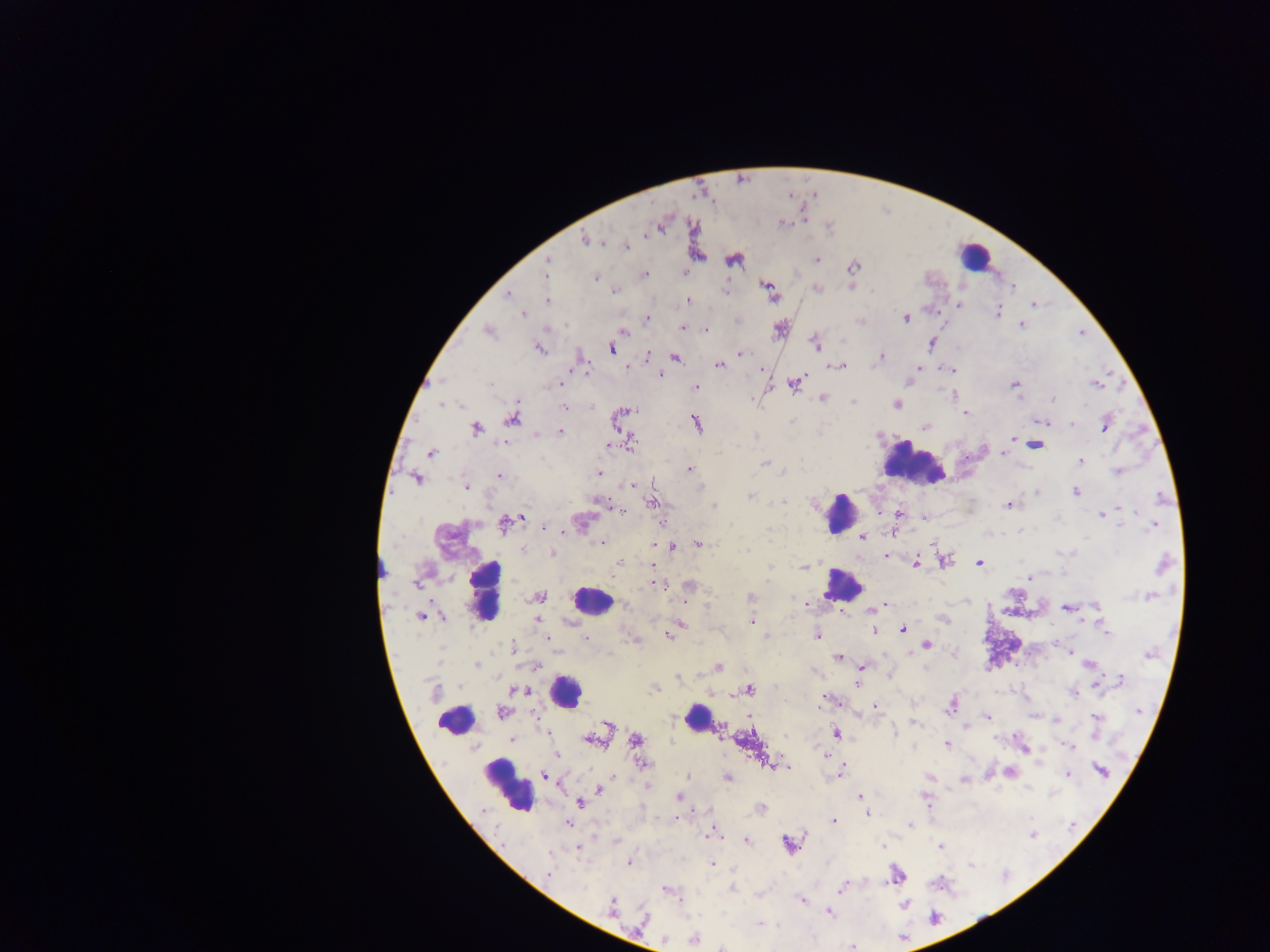

Approximate centers as {x, y} in pixels.
Summary:
  - Malaria parasite locations: {782, 223}, {585, 239}, {626, 246}, {733, 260}, {816, 260}, {547, 265}, {852, 267}, {685, 272}, {545, 274}, {644, 275}, {596, 278}, {852, 287}, {768, 288}, {817, 288}, {726, 290}, {615, 291}, {507, 294}, {772, 294}, {547, 301}, {688, 301}, {959, 304}, {1034, 305}, {998, 312}, {523, 314}, {906, 318}, {647, 319}, {860, 321}, {1022, 324}, {683, 328}, {780, 328}, {705, 329}, {489, 332}, {623, 332}, {816, 343}, {931, 343}, {539, 349}, {612, 349}, {742, 354}, {646, 357}, {675, 357}, {881, 357}, {719, 365}, {840, 366}, {628, 367}, {917, 367}, {473, 369}, {951, 370}, {660, 375}, {562, 380}, {441, 381}, {559, 384}, {795, 384}, {1096, 384}, {1014, 385}, {696, 387}, {823, 397}, {1053, 398}, {853, 402}, {441, 404}, {897, 404}, {461, 405}, {564, 407}, {628, 411}, {966, 413}, {511, 418}, {1041, 421}, {697, 424}, {1072, 424}, {1105, 425}, {925, 426}, {476, 429}, {560, 432}, {535, 433}, {1012, 439}, {631, 441}, {1017, 441}, {503, 443}, {1036, 444}, {608, 445}, {431, 453}, {1003, 455}, {1080, 461}, {766, 463}, {689, 469}, {783, 472}, {1118, 472}, {598, 473}, {500, 475}, {416, 479}, {633, 485}, {465, 487}, {1076, 492}, {1037, 493}, {750, 495}, {1163, 499}, {597, 501}, {782, 501}, {652, 503}, {1008, 505}, {713, 506}, {621, 512}, {898, 514}, {1102, 515}, {522, 517}, {1118, 524}, {503, 525}, {1152, 526}, {545, 527}, {1019, 530}, {862, 538}, {601, 542}, {698, 544}, {672, 547}, {523, 549}, {748, 551}, {552, 553}, {886, 556}, {944, 561}, {619, 563}, {916, 563}, {980, 564}, {652, 565}, {1162, 565}, {804, 567}, {1030, 578}, {416, 585}, {660, 585}, {688, 585}, {539, 597}, {751, 597}, {1150, 597}, {803, 603}, {882, 606}, {1097, 606}, {1067, 608}, {874, 609}, {420, 617}, {442, 618}, {942, 618}, {537, 621}, {751, 622}, {680, 623}, {903, 629}, {1107, 630}, {876, 631}, {818, 635}, {669, 636}, {765, 636}, {547, 638}, {586, 638}, {926, 645}, {512, 648}, {1068, 653}, {1150, 654}, {839, 657}, {1089, 664}, {477, 665}, {537, 666}, {718, 667}, {862, 667}, {678, 677}, {1121, 680}, {857, 683}, {655, 688}, {749, 689}, {519, 690}, {435, 692}, {1073, 693}, {825, 700}, {951, 706}, {875, 707}, {1139, 711}, {501, 713}, {987, 717}, {1096, 718}, {915, 722}, {608, 725}, {893, 732}, {837, 733}, {511, 740}, {636, 740}, {592, 741}, {947, 744}, {1068, 747}, {826, 754}, {557, 755}, {642, 763}, {771, 763}, {780, 766}, {787, 768}, {1101, 771}, {840, 772}, {1010, 772}, {1068, 775}, {545, 776}, {688, 777}, {929, 777}, {727, 778}, {963, 779}, {647, 787}, {600, 790}, {678, 796}, {860, 796}, {579, 802}, {761, 808}, {868, 814}, {834, 822}, {568, 824}, {910, 824}, {712, 833}, {1033, 835}, {615, 841}, {746, 841}, {789, 844}, {883, 846}, {939, 846}, {578, 849}, {628, 863}, {712, 864}, {549, 873}, {896, 876}, {842, 887}, {732, 888}, {667, 891}, {801, 900}, {904, 904}, {611, 906}, {829, 912}, {935, 917}, {643, 920}, {759, 924}, {695, 939}, {723, 947}, {852, 947}
  - Leukocyte locations (subset; some below the resolvable size): {974, 254}, {914, 464}, {840, 512}, {381, 565}, {842, 584}, {486, 592}, {591, 600}, {566, 692}, {698, 718}, {455, 720}, {508, 785}
  - Country: Ghana
  - Image size: 1270×952 pixels
  - Preparation: thick blood smear
  - Capture: mobile-phone photograph through a microscope
  - Field of view: single